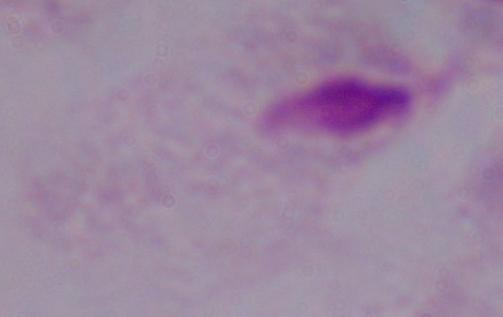

Summary:
  - Magnification: 1000x
  - Identification: trichomonad
  - Modality: photomicrograph